Assess for malaria.
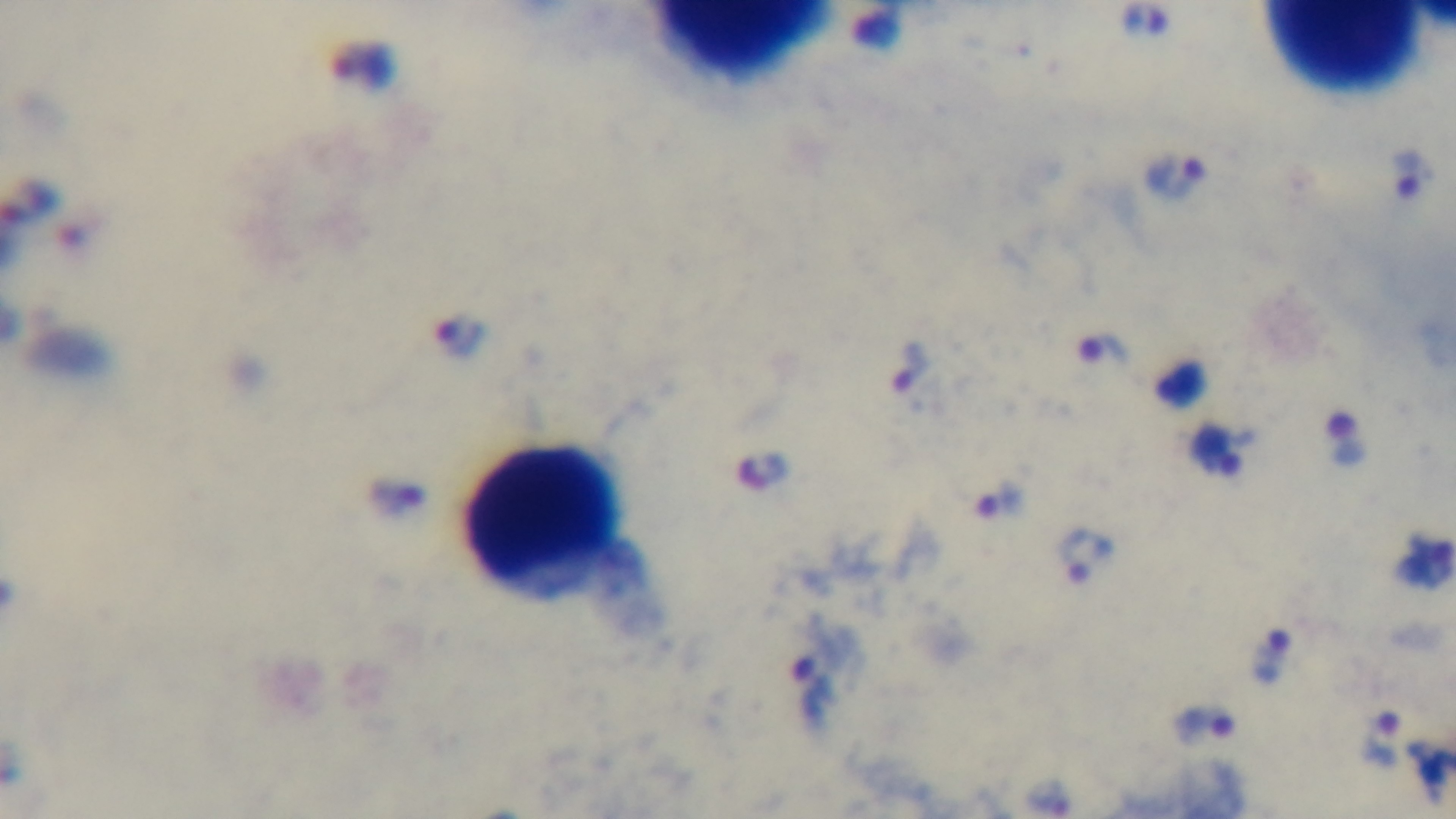
It is infected.

{
  "stain": "Giemsa",
  "modality": "light microscopy",
  "capture": "mounted 4K digital camera",
  "preparation": "thick",
  "objective": "100x oil immersion",
  "field_of_view": "single"
}